Identify the blood parasite species.
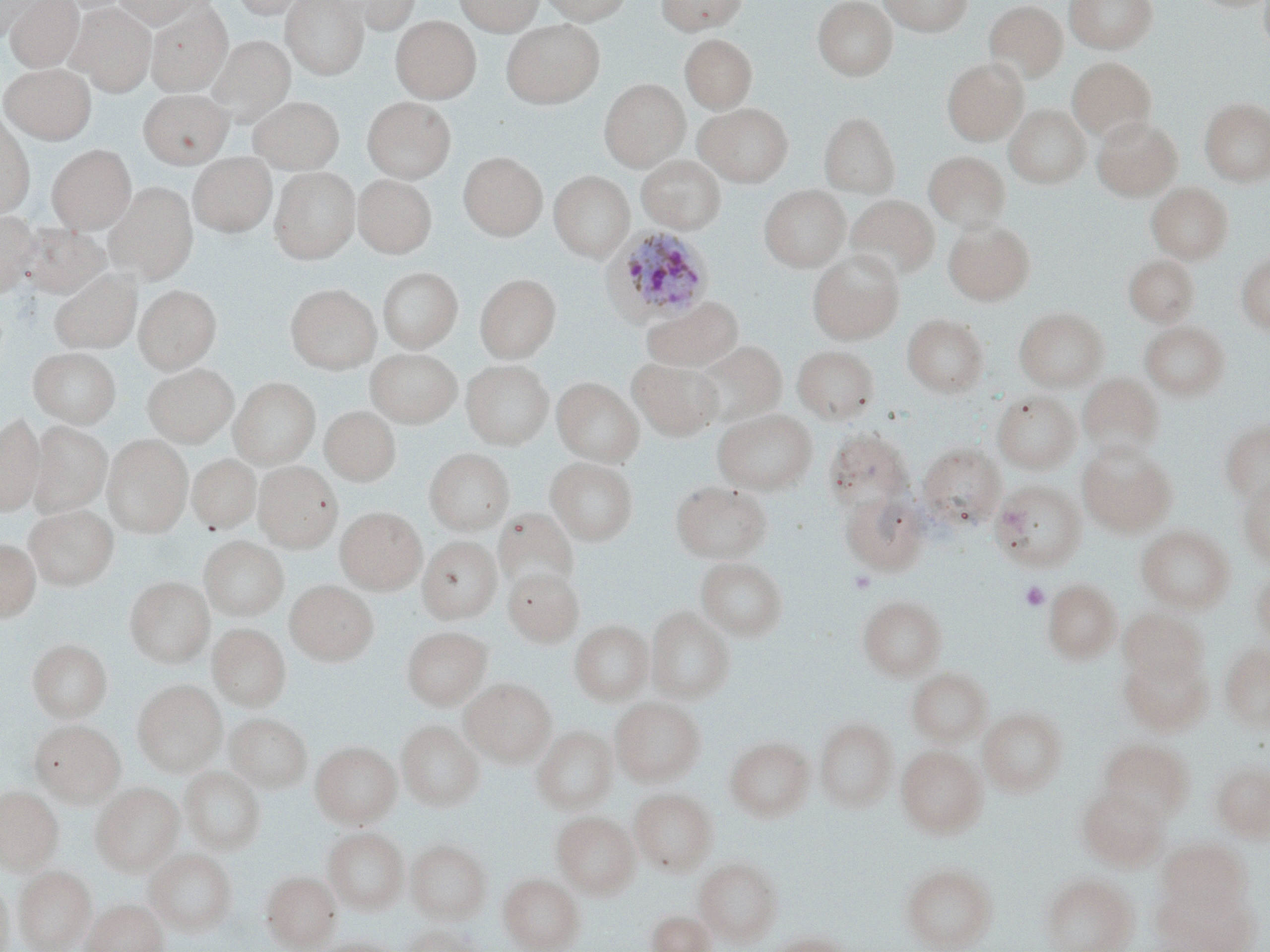
Plasmodium ovale.

{
  "uninfected_red_blood_cell_locations": "approximate bounding boxes as [x1, y1, x2, y2] in pixels: [1, 0, 42, 40], [4, 0, 83, 72], [113, 0, 208, 29], [231, 0, 313, 19], [281, 0, 368, 79], [336, 0, 422, 33], [454, 0, 543, 35], [539, 0, 632, 25], [656, 0, 747, 34], [812, 0, 898, 80], [879, 0, 974, 35], [1065, 0, 1157, 53], [1259, 0, 1270, 56], [984, 1, 1067, 82], [68, 2, 156, 95], [146, 3, 232, 95], [391, 16, 480, 102], [501, 20, 605, 108], [680, 33, 757, 112], [208, 36, 294, 123], [1067, 57, 1156, 141], [942, 58, 1028, 145], [1, 64, 96, 143], [599, 78, 689, 171], [139, 88, 232, 167], [249, 96, 344, 172], [362, 97, 455, 182], [1199, 97, 1270, 186], [694, 102, 793, 186], [1004, 104, 1090, 188], [819, 112, 899, 197], [0, 114, 34, 219], [1092, 116, 1182, 201], [47, 144, 136, 233], [924, 150, 1010, 231], [459, 152, 547, 240], [189, 153, 276, 237], [637, 155, 725, 233], [270, 166, 359, 264], [549, 171, 634, 261], [353, 175, 436, 258], [1147, 182, 1233, 263], [105, 183, 198, 282], [759, 185, 850, 271], [846, 194, 940, 280], [0, 211, 41, 297], [944, 220, 1035, 305], [18, 222, 109, 298], [807, 250, 904, 344], [1235, 253, 1270, 333], [1124, 254, 1199, 327], [378, 267, 462, 352], [50, 271, 141, 353], [475, 273, 560, 362], [286, 284, 381, 374], [134, 285, 221, 373], [642, 296, 743, 372], [1014, 307, 1109, 391], [902, 314, 988, 397], [1139, 321, 1230, 400], [693, 340, 787, 427], [792, 345, 879, 424], [28, 347, 121, 428], [366, 348, 462, 427], [629, 358, 722, 440], [461, 359, 554, 449], [143, 363, 238, 447], [1078, 372, 1163, 457], [230, 377, 319, 469], [552, 377, 644, 466], [993, 391, 1081, 473], [320, 406, 400, 486], [712, 408, 818, 494], [0, 413, 44, 516], [1220, 420, 1270, 503], [28, 421, 111, 517], [824, 429, 912, 513], [103, 434, 193, 537], [1077, 441, 1176, 536], [918, 443, 1005, 529], [425, 448, 514, 534], [188, 454, 259, 533], [546, 457, 638, 545], [254, 461, 342, 551], [1237, 476, 1270, 567], [990, 480, 1086, 571], [672, 481, 771, 563], [840, 490, 928, 575], [25, 504, 118, 589], [335, 507, 427, 594], [494, 508, 577, 592], [1135, 525, 1235, 613], [199, 536, 289, 620], [418, 536, 502, 622], [0, 540, 40, 621], [696, 557, 787, 640], [504, 568, 583, 646], [1250, 568, 1270, 645], [125, 576, 213, 666], [1042, 578, 1122, 663], [285, 580, 378, 666], [858, 595, 947, 680], [646, 606, 734, 703], [1119, 608, 1209, 688], [570, 620, 654, 704], [208, 623, 290, 710], [402, 626, 492, 710], [28, 639, 112, 722], [1220, 644, 1270, 730], [1119, 649, 1212, 735], [907, 667, 992, 747], [460, 678, 557, 766], [133, 680, 226, 775], [610, 697, 705, 785], [979, 707, 1068, 797], [225, 713, 311, 792], [815, 717, 898, 812], [397, 719, 484, 810], [31, 720, 125, 806], [531, 725, 618, 814], [725, 737, 815, 821], [1098, 738, 1193, 820], [310, 741, 402, 828], [896, 745, 988, 838], [1212, 761, 1270, 840], [180, 767, 265, 854], [91, 782, 184, 876], [1076, 783, 1169, 871], [0, 786, 62, 872], [629, 788, 718, 875], [552, 810, 640, 898], [323, 827, 408, 914], [406, 839, 491, 923], [1158, 840, 1250, 916], [145, 848, 237, 936], [694, 856, 782, 944], [900, 863, 997, 952], [14, 865, 95, 951], [262, 871, 341, 951], [499, 873, 584, 952], [1041, 873, 1138, 952], [0, 877, 12, 952], [1162, 888, 1259, 950], [82, 898, 167, 952], [647, 910, 714, 952], [404, 924, 484, 952], [766, 933, 853, 952], [314, 938, 402, 952]",
  "modality": "light microscopy",
  "stain": "May-Grünwald-Giemsa",
  "preparation": "thin blood film",
  "field_of_view": "single",
  "magnification": "1000x",
  "platelet_locations": "approximate bounding boxes as [x1, y1, x2, y2] in pixels: [1020, 581, 1050, 611]",
  "image_size": "1270×952 pixels",
  "plasmodium_ovale_infected_red_blood_cell_locations": "approximate bounding boxes as [x1, y1, x2, y2] in pixels: [604, 225, 715, 327]"
}